State which cell type is depicted.
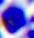
This is a leukocyte.

Summary:
  - Modality: photomicrograph
  - Magnification: 400x